Assess this cell for malaria.
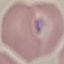

It is parasitized.

Summary:
  - Stain: Giemsa
  - Preparation: thin blood film
  - Capture: smartphone through the microscope eyepiece
  - Image type: cell patch, automatically extracted from a larger field of view and resized to 64 × 64 pixels